State which cell type is depicted.
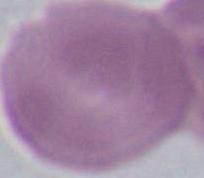

This is an erythrocyte.

Summary:
  - Magnification: 1000x
  - Modality: micrograph